Name the parasite shown.
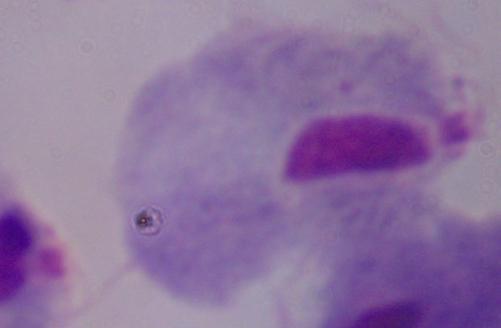

This is a trichomonad.

modality = photomicrograph
magnification = 1000x